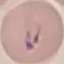
malaria status = parasitized
preparation = thin blood smear
image type = cell patch, automatically extracted from a larger field of view and resized to 64 × 64 pixels
capture = smartphone through the microscope eyepiece
stain = Giemsa